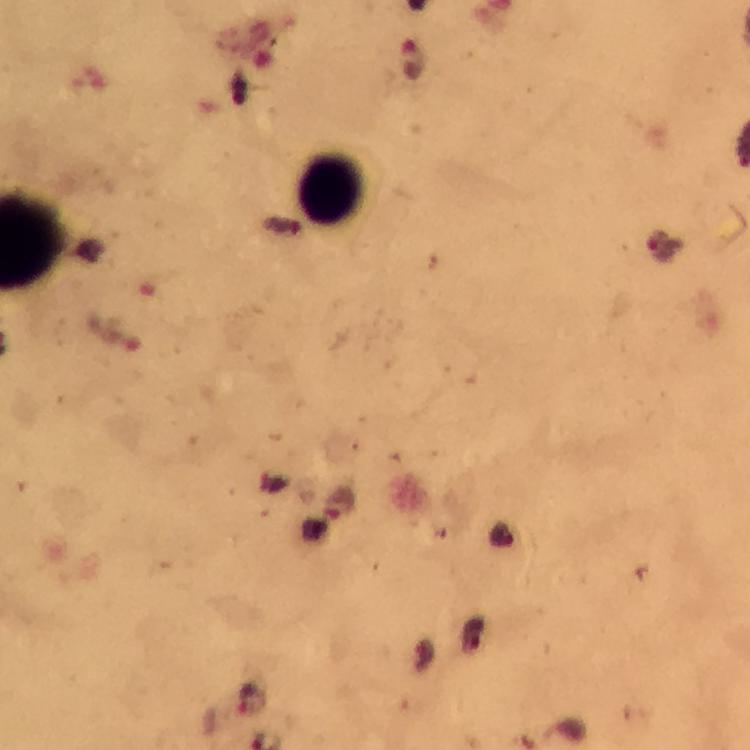

Approximate centers as {x, y} in pixels.
Summary:
  - Leukocyte locations: {332, 191}
  - Malaria parasite locations: {411, 61}, {339, 505}
  - Capture: smartphone camera through the microscope
  - Magnification: 100x
  - Immersion oil: used
  - Image size: 750×750 pixels
  - Context: from a diagnostic examination for malaria
  - Cropped from: a single field of view
  - Stain: Giemsa
  - Preparation: thick blood film